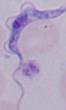

identification = trypanosome
magnification = 1000x
modality = photomicrograph